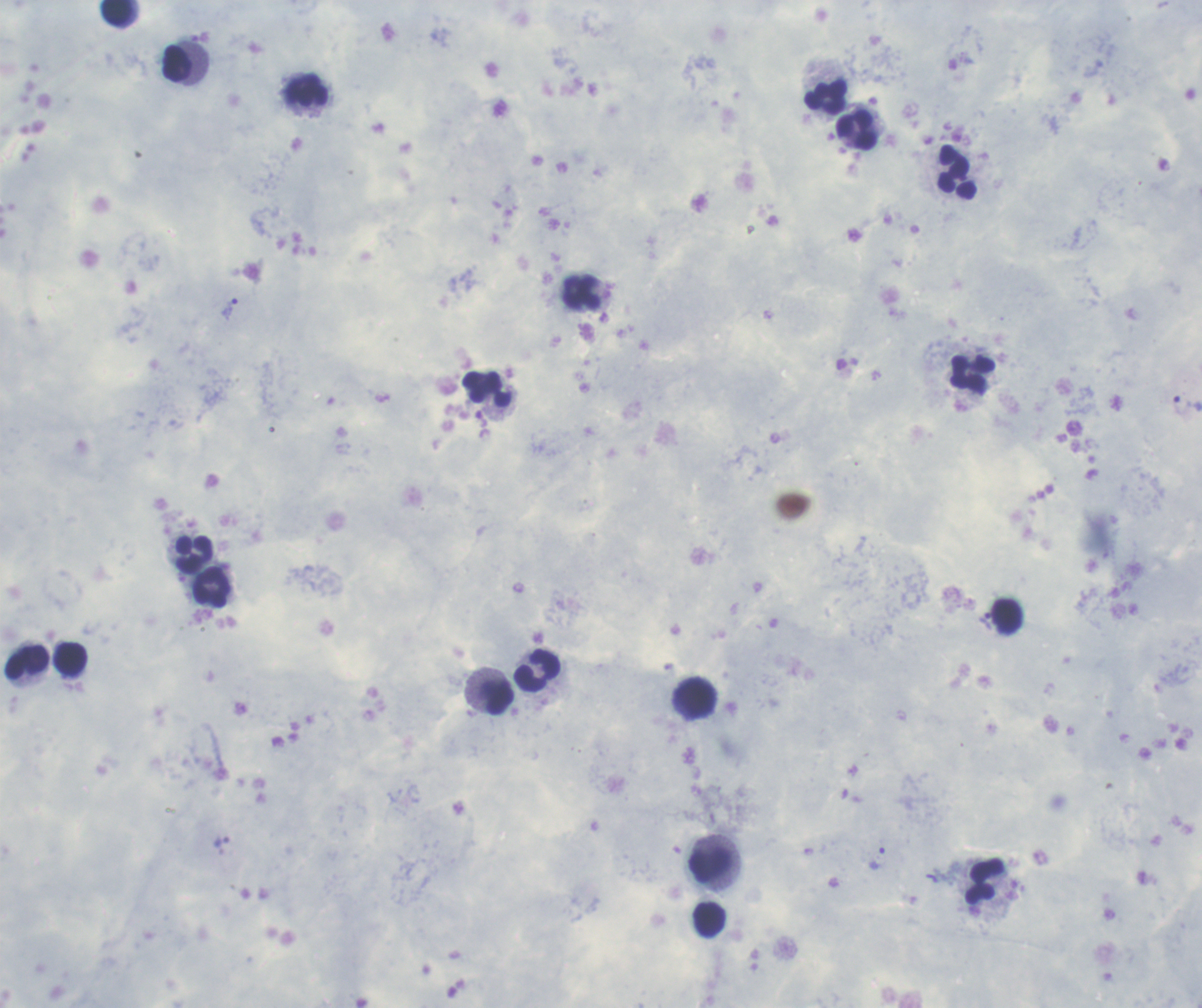

Approximate centers as {x, y} in pixels. Leukocyte locations: {117, 12}, {176, 62}, {307, 91}, {824, 96}, {856, 130}, {957, 173}, {582, 292}, {973, 374}, {488, 389}, {194, 553}, {211, 587}, {1007, 615}, {70, 659}, {28, 662}, {538, 671}, {497, 697}, {697, 698}, {711, 865}, {986, 882}, {708, 920}. Trophozoite locations: {229, 309}, {877, 858}. Previously used in an actual diagnosis. Coloration quality: good. One field from this slide. Thick blood smear. Romanowsky-stained preparation. Background quality: good. Image is 1202×1008 pixels. Result: Plasmodium parasites detected. 100x magnification.